Report the malaria status of this cell.
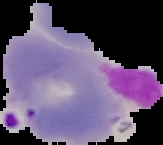

It is parasitized.

preparation = thin blood film
image type = segmented cell region on a black background
image size = 163×145 pixels